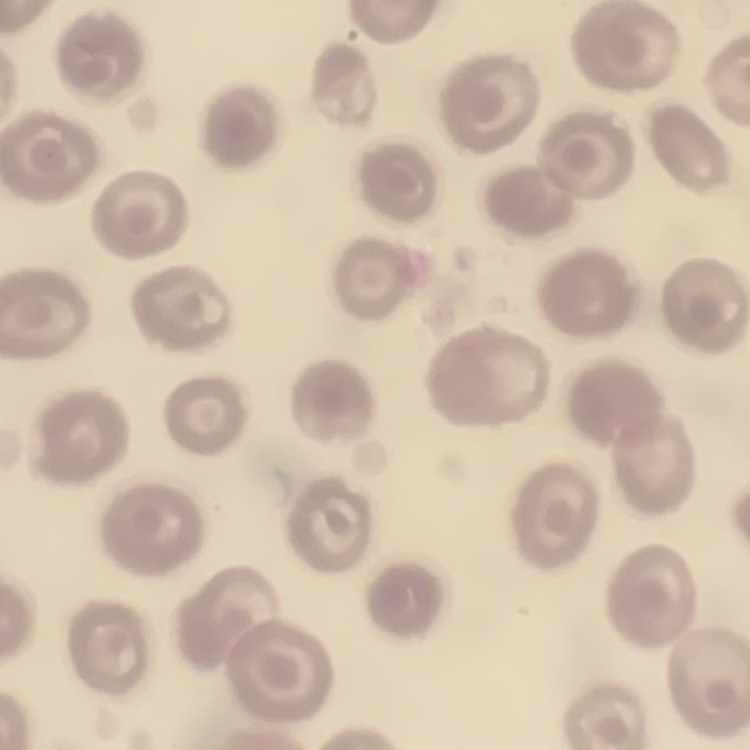
erythrocyte morphology = no rouleaux formation
image type = square crop of a larger photomicrograph
stain = Field's or Giemsa
preparation = thin peripheral smear